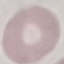
{
  "result": "no malaria parasites seen",
  "stain": "Giemsa",
  "capture": "smartphone camera at the microscope eyepiece",
  "preparation": "thin smear",
  "image_type": "cell patch, automatically extracted from a larger field of view and resized to 64 × 64 pixels"
}